Name the parasite shown.
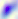
This is Toxoplasma gondii.

magnification: 400x
modality: micrograph